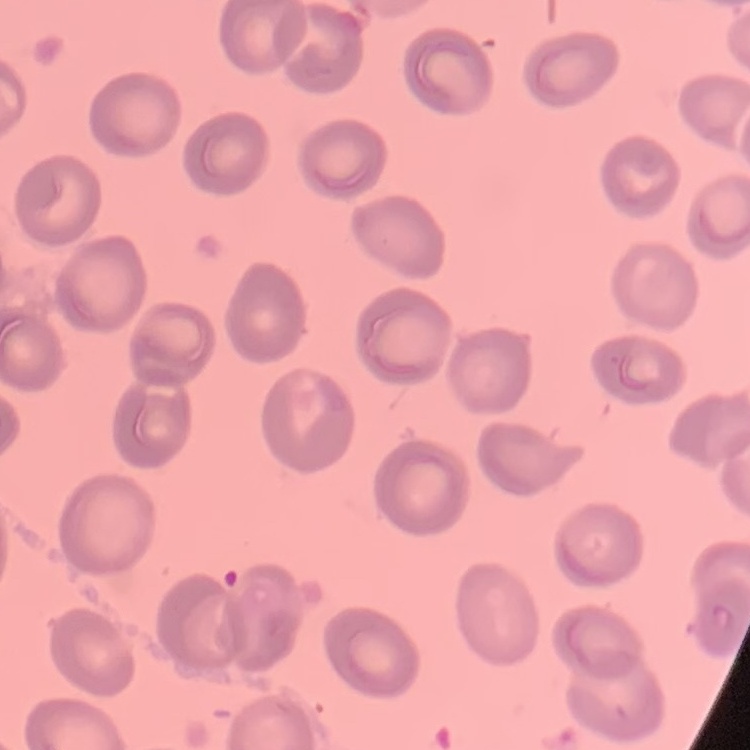

red blood cell morphology = no rouleaux formation
stain = Field's or Giemsa
image type = one tile cut from a larger photomicrograph
preparation = thin blood film